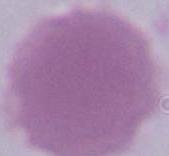 An erythrocyte is shown. Micrograph. 1000x magnification.